Identify the cell.
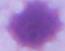

This is an erythrocyte.

modality = photomicrograph
magnification = 1000x